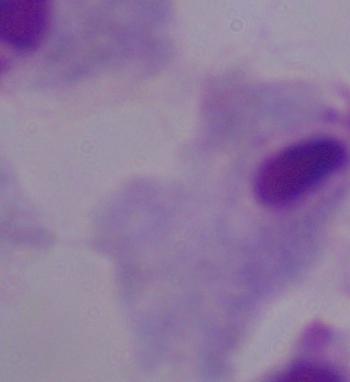
Summary:
  - Identification: trichomonad
  - Magnification: 1000x
  - Modality: micrograph